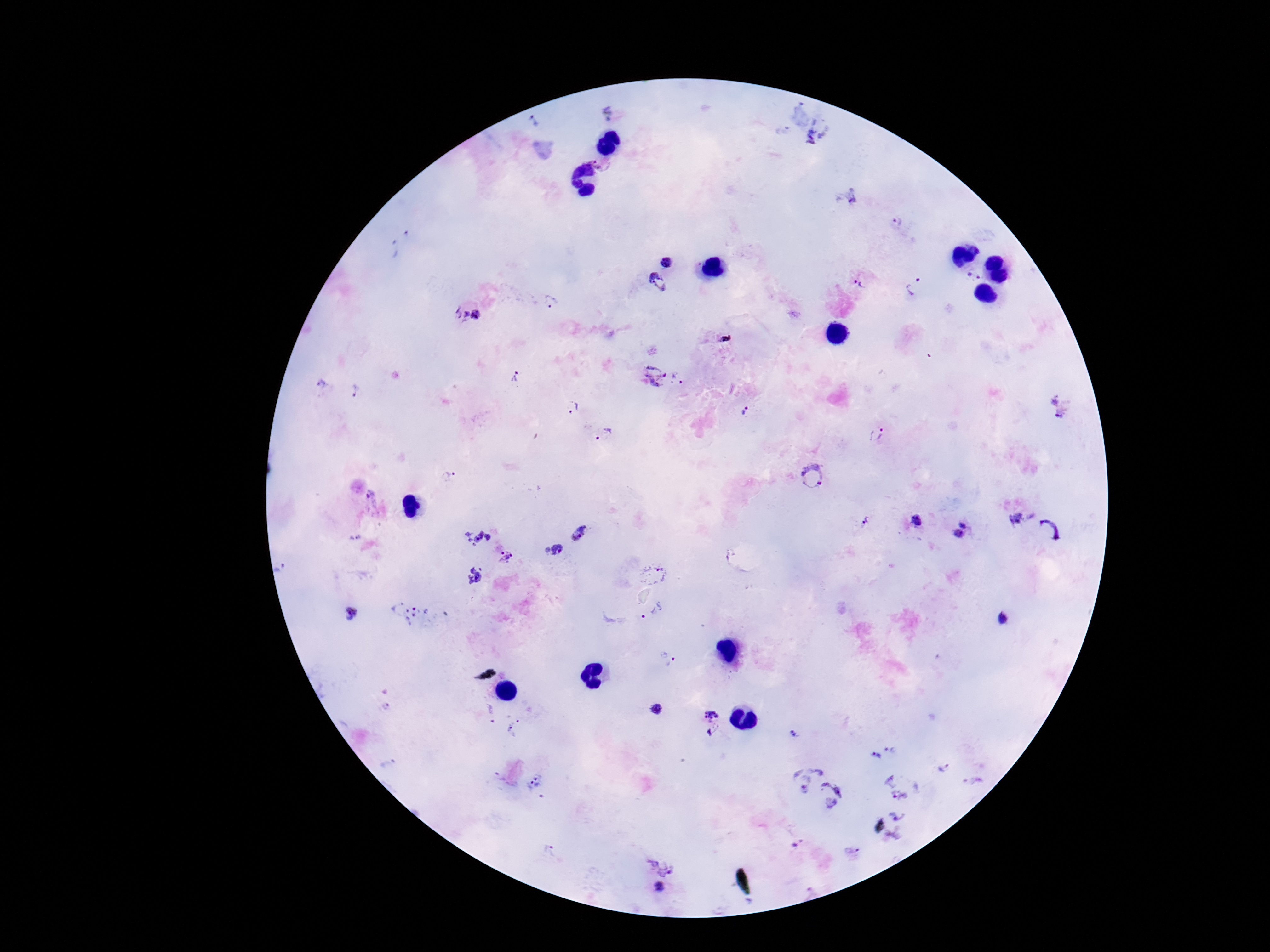
Approximate object centers, in pixels from the top-left corner.
Summary:
  - Plasmodium parasite locations: (x=609, y=112), (x=534, y=122), (x=818, y=131), (x=600, y=159), (x=850, y=197), (x=896, y=220), (x=391, y=249), (x=666, y=262), (x=974, y=275), (x=657, y=282), (x=860, y=282), (x=914, y=286), (x=550, y=300), (x=467, y=314), (x=654, y=373), (x=515, y=376), (x=678, y=376), (x=320, y=384), (x=357, y=392), (x=1059, y=405), (x=572, y=407), (x=748, y=411), (x=605, y=434), (x=877, y=434), (x=447, y=476), (x=813, y=476), (x=371, y=497), (x=1017, y=518), (x=864, y=521), (x=917, y=521), (x=963, y=523), (x=1049, y=530), (x=477, y=533), (x=579, y=533), (x=958, y=534), (x=356, y=538), (x=555, y=551), (x=507, y=556), (x=279, y=569), (x=654, y=573), (x=474, y=576), (x=411, y=612), (x=649, y=612), (x=351, y=614), (x=1004, y=619), (x=664, y=657), (x=386, y=708), (x=658, y=709), (x=712, y=722), (x=512, y=727), (x=793, y=735), (x=894, y=747), (x=874, y=756), (x=943, y=769), (x=804, y=776), (x=971, y=780), (x=535, y=785), (x=896, y=785), (x=833, y=794), (x=900, y=830), (x=797, y=843), (x=552, y=852), (x=851, y=853), (x=660, y=865), (x=661, y=887)
  - Field of view: one from this slide
  - Image size: 1270×952 pixels
  - Capture: smartphone camera through the microscope eyepiece
  - Magnification: 100x
  - Preparation: thick blood smear
  - Stain: Giemsa
  - Patient malaria status: positive